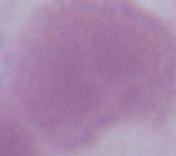
Summary:
  - Modality: micrograph
  - Identification: red blood cell
  - Magnification: 1000x